Identify the cell.
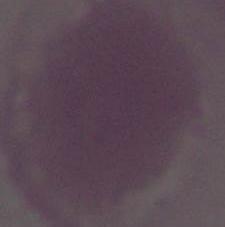
This is an erythrocyte.

Captured at 1000x magnification. Micrograph.